Identify the blood parasite species.
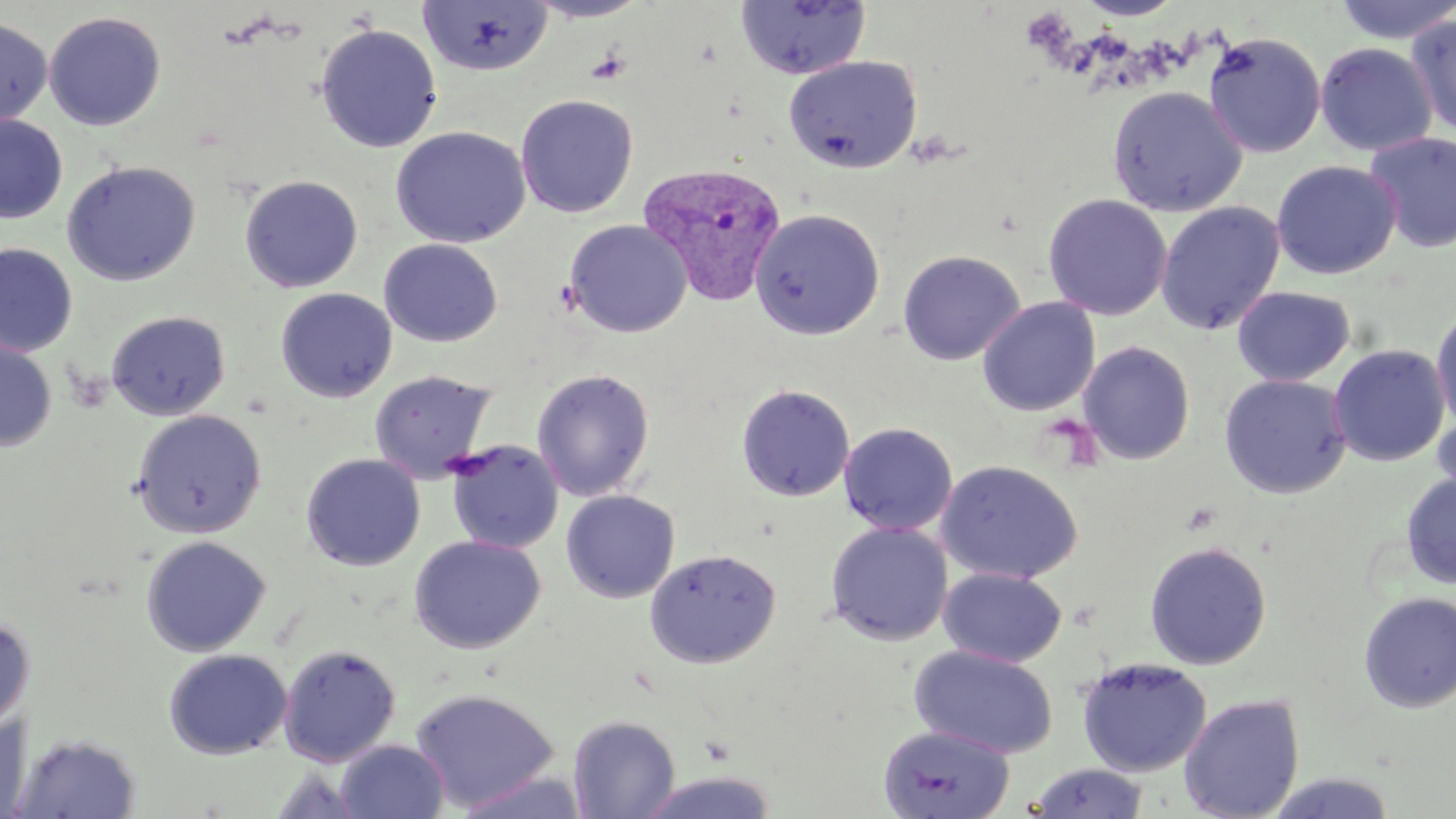

Plasmodium vivax.

Approximate bounding boxes as (x1, y1, x2, y2) in pixels. Uninfected red blood cell locations: (524, 0, 652, 23), (1074, 0, 1186, 21), (1333, 0, 1456, 45), (417, 1, 553, 76), (734, 1, 872, 80), (44, 11, 166, 130), (1406, 11, 1456, 140), (0, 17, 53, 127), (315, 23, 442, 153), (1203, 31, 1326, 158), (1315, 42, 1437, 157), (783, 55, 922, 174), (1107, 86, 1247, 217), (515, 94, 638, 218), (0, 115, 68, 224), (390, 126, 530, 248), (1364, 133, 1456, 252), (61, 160, 200, 286), (1271, 160, 1401, 280), (240, 175, 363, 293), (1042, 193, 1172, 320), (1156, 201, 1285, 335), (750, 207, 886, 340), (564, 219, 692, 338), (379, 239, 503, 346), (0, 243, 77, 357), (897, 249, 1025, 365), (1232, 286, 1355, 386), (275, 288, 397, 402), (977, 297, 1100, 416), (1431, 306, 1456, 433), (106, 310, 230, 420), (0, 336, 56, 452), (1078, 341, 1196, 465), (1328, 344, 1450, 467), (532, 368, 655, 501), (369, 370, 496, 484), (1219, 374, 1353, 499), (735, 384, 855, 502), (132, 408, 267, 538), (1432, 409, 1456, 511), (839, 422, 958, 535), (445, 439, 563, 554), (301, 453, 425, 571), (936, 459, 1083, 584), (1400, 473, 1456, 591), (561, 490, 680, 603), (825, 521, 953, 645), (409, 535, 546, 654), (141, 536, 270, 656), (1144, 540, 1272, 670), (644, 548, 781, 669), (938, 566, 1067, 667), (1357, 591, 1456, 713), (0, 617, 34, 730), (279, 644, 400, 766), (910, 644, 1059, 759), (164, 649, 292, 759), (1076, 657, 1212, 777), (410, 688, 560, 811), (1179, 693, 1305, 819), (0, 714, 32, 818), (568, 715, 680, 818), (878, 725, 1015, 819), (11, 734, 142, 818), (335, 740, 450, 819), (1028, 763, 1150, 818), (268, 766, 367, 818), (634, 770, 780, 818), (456, 771, 589, 819), (1263, 771, 1399, 818). Platelet locations: (1022, 8, 1076, 54), (584, 48, 631, 85). Plasmodium vivax-infected red blood cell locations: (634, 164, 786, 306). Light microscopy. May-Grünwald-Giemsa stain. Captured at 1000x magnification. Single field of view. Image is 1456×819 pixels. Thin blood film.